State the preparation type.
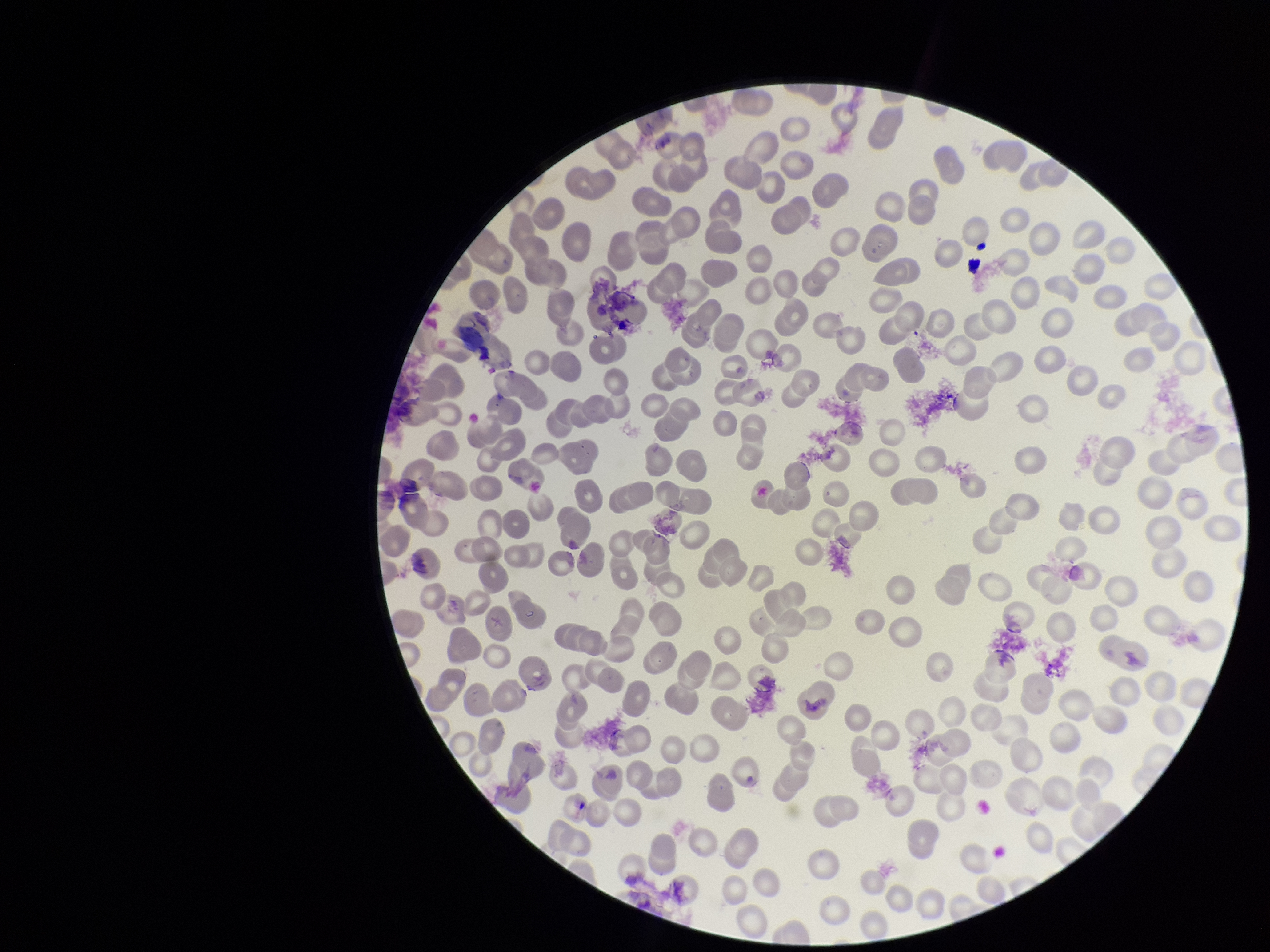
A thin smear.

Summary:
  - Field of view: one from this slide
  - Patient malaria status: negative
  - Red blood cell count: 186
  - Stain: Giemsa
  - Parasitized red blood cells: none detected
  - Capture: smartphone photograph through the microscope eyepiece
  - Image size: 1270×952 pixels
  - Parasitized red blood cell count: 0